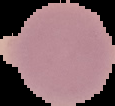
preparation = thin blood film
malaria status = uninfected
image size = 115×106 pixels
image type = cell region segmented out of the field of view; surrounding area masked to black